Classify this cell by malaria status.
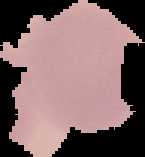

It is uninfected.

Segmented cell region on a black background. Image is 145×157 pixels. From a thin blood film.